State which parasite is depicted.
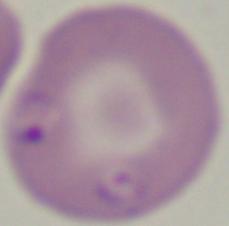
Babesia.

Captured at 1000x magnification. Micrograph.